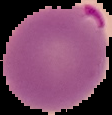

image type = cell region segmented out of the field of view; surrounding area masked to black
preparation = thin blood smear
malaria status = parasitized
image size = 112×115 pixels